State which cell type is depicted.
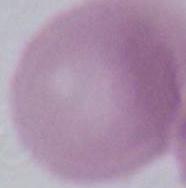

This is an erythrocyte.

modality = photomicrograph
magnification = 1000x